Identify the blood parasite species.
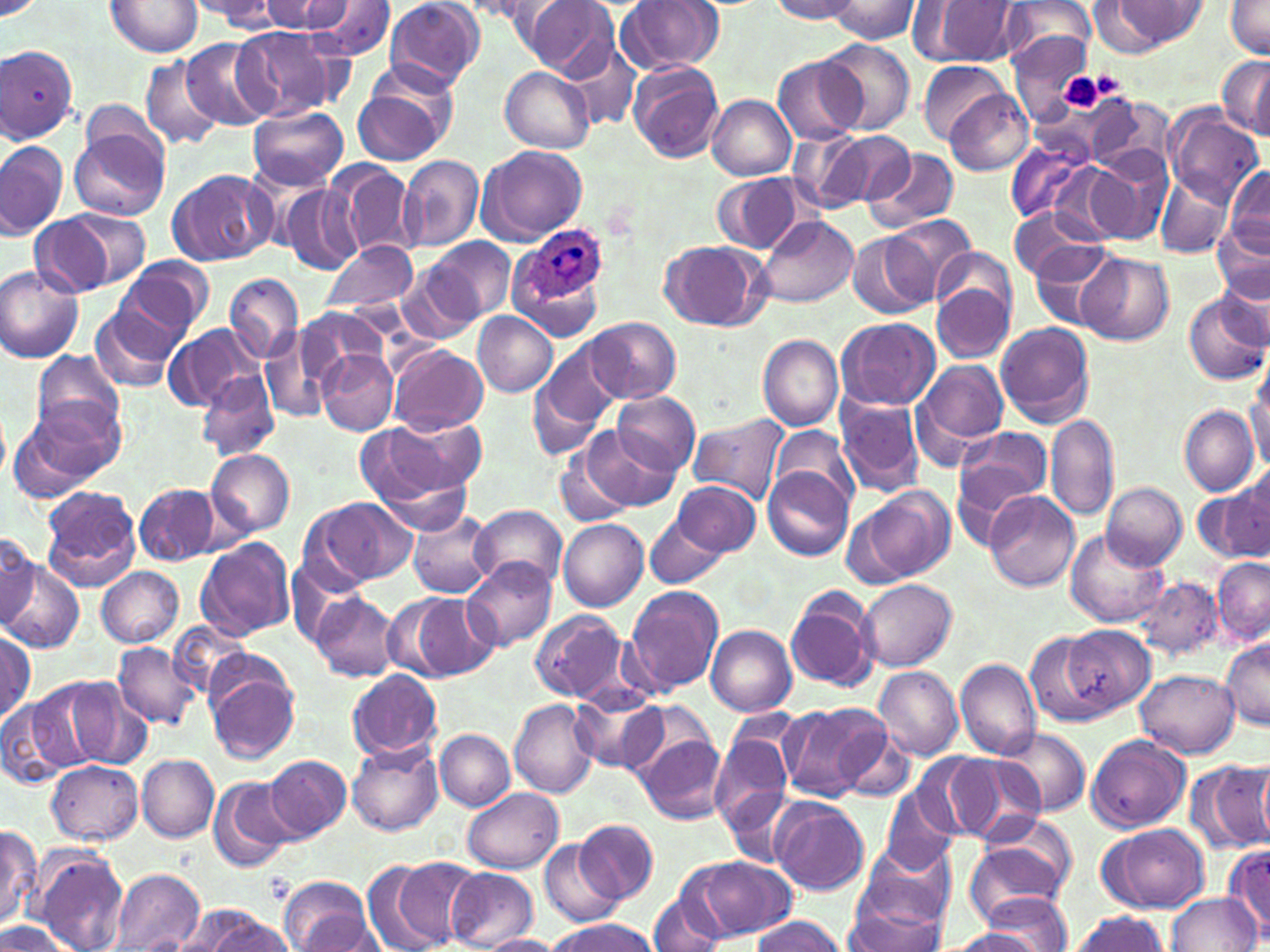
Plasmodium ovale.

Summary:
  - Coordinate format: approximate bounding boxes as (x1, y1, x2, y2) in pixels
  - Uninfected red blood cell locations: (261, 0, 353, 34), (312, 0, 398, 60), (386, 0, 484, 90), (524, 0, 619, 81), (616, 0, 723, 76), (770, 0, 865, 22), (826, 0, 921, 43), (0, 1, 45, 22), (104, 1, 202, 57), (197, 1, 287, 31), (919, 1, 1021, 65), (997, 1, 1096, 75), (1223, 1, 1270, 58), (458, 2, 546, 21), (1108, 3, 1207, 47), (233, 26, 342, 118), (1011, 33, 1094, 126), (183, 37, 275, 130), (820, 39, 914, 133), (565, 40, 642, 133), (0, 45, 77, 143), (1215, 54, 1270, 139), (140, 55, 223, 151), (773, 55, 862, 145), (917, 59, 1008, 144), (628, 60, 725, 163), (499, 65, 592, 153), (353, 74, 455, 166), (945, 90, 1033, 176), (708, 95, 795, 180), (1084, 95, 1158, 174), (79, 101, 170, 174), (250, 105, 349, 190), (1166, 109, 1263, 206), (72, 126, 168, 223), (793, 126, 913, 215), (1005, 136, 1094, 225), (0, 140, 68, 239), (476, 145, 588, 245), (864, 147, 961, 232), (1092, 148, 1172, 244), (398, 155, 484, 254), (1048, 160, 1137, 245), (328, 161, 416, 259), (1225, 167, 1269, 256), (168, 169, 275, 265), (711, 172, 807, 255), (1155, 174, 1233, 257), (278, 185, 363, 275), (1007, 207, 1106, 283), (63, 208, 151, 290), (887, 212, 976, 303), (28, 215, 114, 301), (754, 215, 857, 309), (1211, 217, 1269, 304), (848, 234, 934, 318), (428, 237, 514, 322), (323, 240, 417, 313), (660, 242, 765, 331), (1030, 242, 1118, 318), (935, 248, 1015, 320), (1078, 253, 1174, 344), (115, 257, 213, 341), (0, 265, 85, 364), (1214, 268, 1269, 348), (225, 274, 303, 364), (397, 275, 477, 344), (931, 282, 1014, 365), (1185, 291, 1268, 384), (90, 304, 179, 391), (296, 311, 385, 387), (472, 312, 558, 398), (585, 316, 680, 404), (835, 316, 941, 411), (995, 321, 1094, 427), (164, 325, 262, 413), (259, 328, 337, 423), (757, 334, 842, 432), (540, 340, 624, 435), (389, 345, 488, 436), (30, 349, 127, 441), (318, 349, 398, 435), (914, 359, 1010, 456), (527, 368, 606, 456), (197, 371, 279, 462), (1248, 377, 1270, 475), (613, 391, 701, 475), (837, 395, 926, 498), (12, 400, 123, 497), (1179, 404, 1260, 497), (688, 414, 790, 504), (388, 416, 486, 495), (1047, 416, 1119, 520), (356, 423, 455, 509), (770, 424, 858, 510), (581, 425, 679, 513), (954, 426, 1053, 515), (555, 444, 635, 528), (205, 449, 296, 538), (762, 466, 853, 560), (1197, 479, 1270, 566), (673, 483, 764, 555), (1104, 483, 1187, 569), (134, 484, 221, 564), (858, 486, 953, 582), (40, 487, 141, 590), (984, 490, 1080, 593), (302, 498, 412, 590), (470, 504, 566, 592), (408, 508, 497, 598), (646, 514, 725, 590), (558, 518, 648, 611), (0, 531, 40, 625), (1065, 531, 1169, 627), (196, 537, 295, 640), (1213, 557, 1270, 643), (463, 559, 556, 650), (2, 561, 83, 654), (96, 566, 183, 647), (1136, 576, 1223, 660), (859, 579, 956, 671), (623, 584, 724, 696), (786, 587, 881, 694), (311, 592, 399, 682), (412, 593, 501, 679), (383, 594, 459, 681), (530, 608, 629, 703), (707, 624, 797, 716), (1063, 624, 1155, 713), (1, 628, 37, 719), (1025, 629, 1115, 725), (1220, 641, 1270, 730), (113, 643, 201, 730), (955, 659, 1040, 757), (206, 667, 300, 764), (875, 667, 962, 759), (347, 669, 442, 761), (1137, 669, 1240, 757), (30, 676, 117, 770), (67, 680, 151, 769), (570, 687, 667, 774), (618, 697, 718, 781), (508, 699, 599, 798), (0, 701, 72, 791), (779, 702, 889, 802), (829, 719, 918, 802), (709, 726, 797, 838), (997, 728, 1091, 814), (434, 729, 514, 810), (634, 730, 727, 825), (1087, 734, 1190, 832), (345, 741, 443, 837), (941, 753, 1045, 846), (137, 754, 219, 842), (266, 755, 351, 840), (1190, 757, 1270, 854), (45, 760, 143, 846), (208, 776, 295, 872), (462, 789, 563, 873), (725, 789, 798, 866), (881, 789, 959, 875), (770, 798, 868, 895), (574, 818, 660, 904), (1099, 822, 1208, 912), (0, 825, 41, 929), (964, 826, 1074, 922), (540, 840, 621, 927), (856, 842, 956, 933), (1222, 845, 1270, 936), (37, 849, 130, 952), (680, 855, 796, 941), (369, 856, 476, 951), (445, 868, 539, 949), (109, 869, 204, 952), (277, 876, 378, 952), (648, 892, 725, 952), (1168, 892, 1259, 951), (843, 893, 948, 952), (975, 893, 1073, 952), (181, 905, 279, 950), (1064, 911, 1168, 951), (750, 916, 847, 952), (0, 918, 75, 952), (544, 919, 659, 952), (944, 928, 1048, 951), (477, 933, 565, 952)
  - Plasmodium ovale-infected red blood cell locations: (521, 230, 608, 305)
  - Platelet locations: (1059, 71, 1107, 113)
  - Field of view: single
  - Stain: May-Grünwald-Giemsa
  - Image size: 1270×952 pixels
  - Magnification: 1000x
  - Modality: light microscopy
  - Preparation: thin blood smear